Locate every malaria parasite.
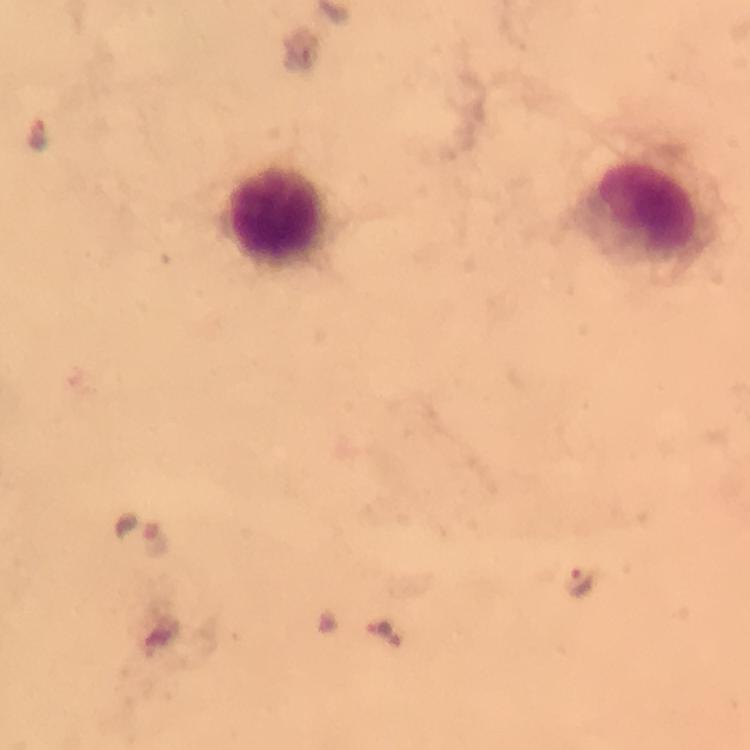

Approximate centers as {x, y} in pixels.
Malaria parasites: {38, 133}, {158, 537}, {584, 579}, {387, 633}.

Leukocyte locations: {276, 211}. From a diagnostic examination for malaria. A crop from one field of view. Giemsa stain. Immersion oil applied. Image is 750×750 pixels. 100x magnification. Smartphone photograph taken through a microscope. Thick smear.